Assess this cell for malaria.
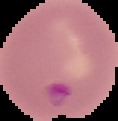

Parasitized.

Summary:
  - Image type: segmented cell region on a black background
  - Preparation: thin blood film
  - Image size: 118×121 pixels